Comment on the morphology of the red blood cells.
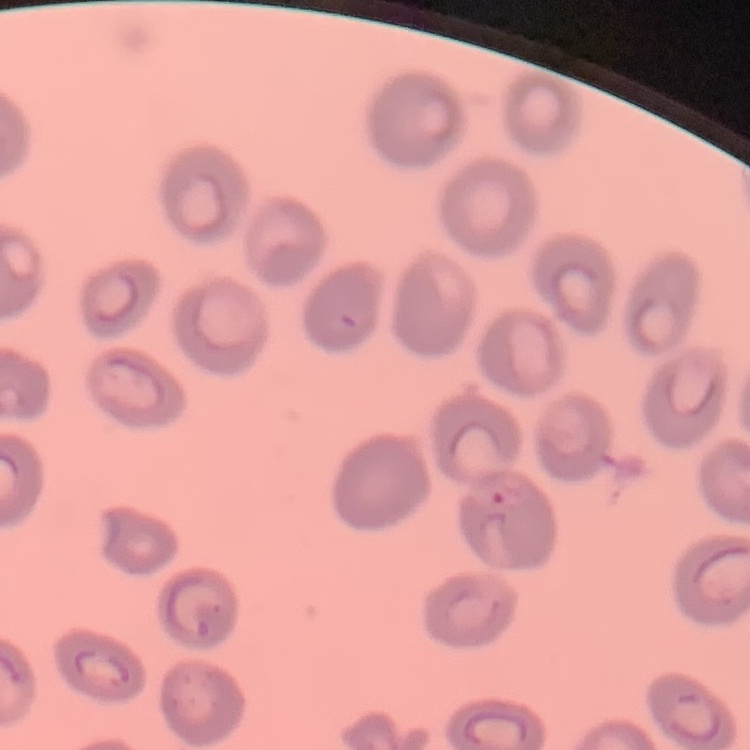

No rouleaux formation.

Summary:
  - Image type: square crop of a larger photomicrograph
  - Preparation: thin peripheral smear
  - Stain: Field's or Giemsa